Outline each blood parasite and name the species.
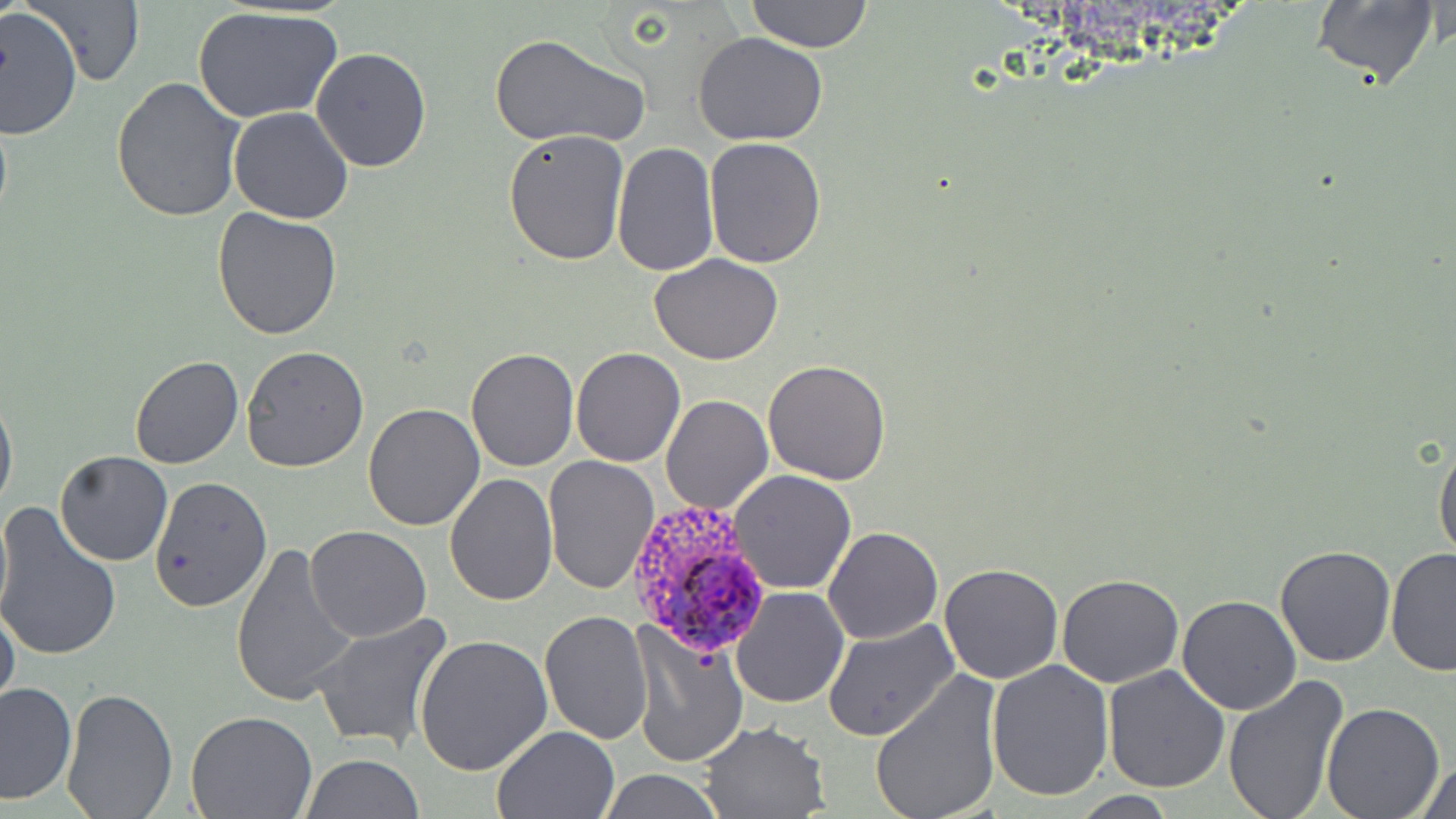

Approximate bounding boxes as [x1, y1, x2, y2] in pixels.
Plasmodium ovale-infected red blood cells: [622, 497, 774, 657].
No Plasmodium falciparum, Plasmodium malariae, Plasmodium vivax, Babesia divergens, or Trypanosoma brucei observed.

slide-level diagnosis = Plasmodium ovale
modality = light microscopy
magnification = 1000x
preparation = thin blood film
uninfected red blood cell locations = approximate bounding boxes as [x1, y1, x2, y2] in pixels: [24, 0, 147, 88], [746, 0, 874, 53], [1308, 0, 1442, 92], [192, 6, 344, 123], [1, 8, 82, 139], [487, 32, 650, 150], [693, 32, 829, 147], [311, 48, 432, 171], [109, 76, 243, 222], [227, 107, 354, 224], [503, 128, 632, 266], [703, 135, 827, 268], [612, 142, 719, 276], [213, 206, 344, 339], [649, 253, 785, 365], [598, 275, 735, 417], [570, 345, 685, 466], [239, 346, 369, 471], [466, 347, 578, 471], [129, 356, 243, 470], [763, 358, 892, 485], [663, 377, 886, 498], [0, 384, 17, 516], [661, 394, 773, 515], [363, 404, 486, 531], [1433, 439, 1456, 564], [54, 450, 174, 566], [543, 456, 661, 595], [727, 469, 857, 594], [444, 474, 559, 608], [148, 476, 273, 613], [0, 501, 12, 631], [0, 504, 122, 664], [821, 526, 944, 645], [306, 527, 432, 643], [229, 542, 358, 707], [1276, 544, 1397, 666], [1384, 549, 1456, 676], [938, 563, 1066, 684], [1058, 575, 1184, 687], [732, 586, 849, 709], [1177, 594, 1303, 715], [0, 603, 20, 714], [538, 610, 654, 743], [311, 613, 453, 753], [823, 618, 959, 742], [630, 623, 749, 771], [415, 636, 554, 777], [984, 659, 1114, 800], [1102, 665, 1232, 793], [872, 670, 1003, 819], [1223, 676, 1348, 819], [0, 682, 76, 804], [60, 685, 178, 817], [1321, 702, 1445, 819], [185, 711, 316, 818], [695, 721, 831, 818], [492, 724, 621, 817], [300, 754, 424, 819], [1413, 758, 1455, 818], [597, 769, 727, 819], [1067, 791, 1185, 819]
field of view = single
image size = 1456×819 pixels
stain = May-Grünwald-Giemsa